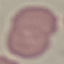

malaria status = uninfected
stain = Giemsa
preparation = thin smear
capture = smartphone through the microscope eyepiece
image type = automatically extracted cell patch, resized to 64 × 64 pixels